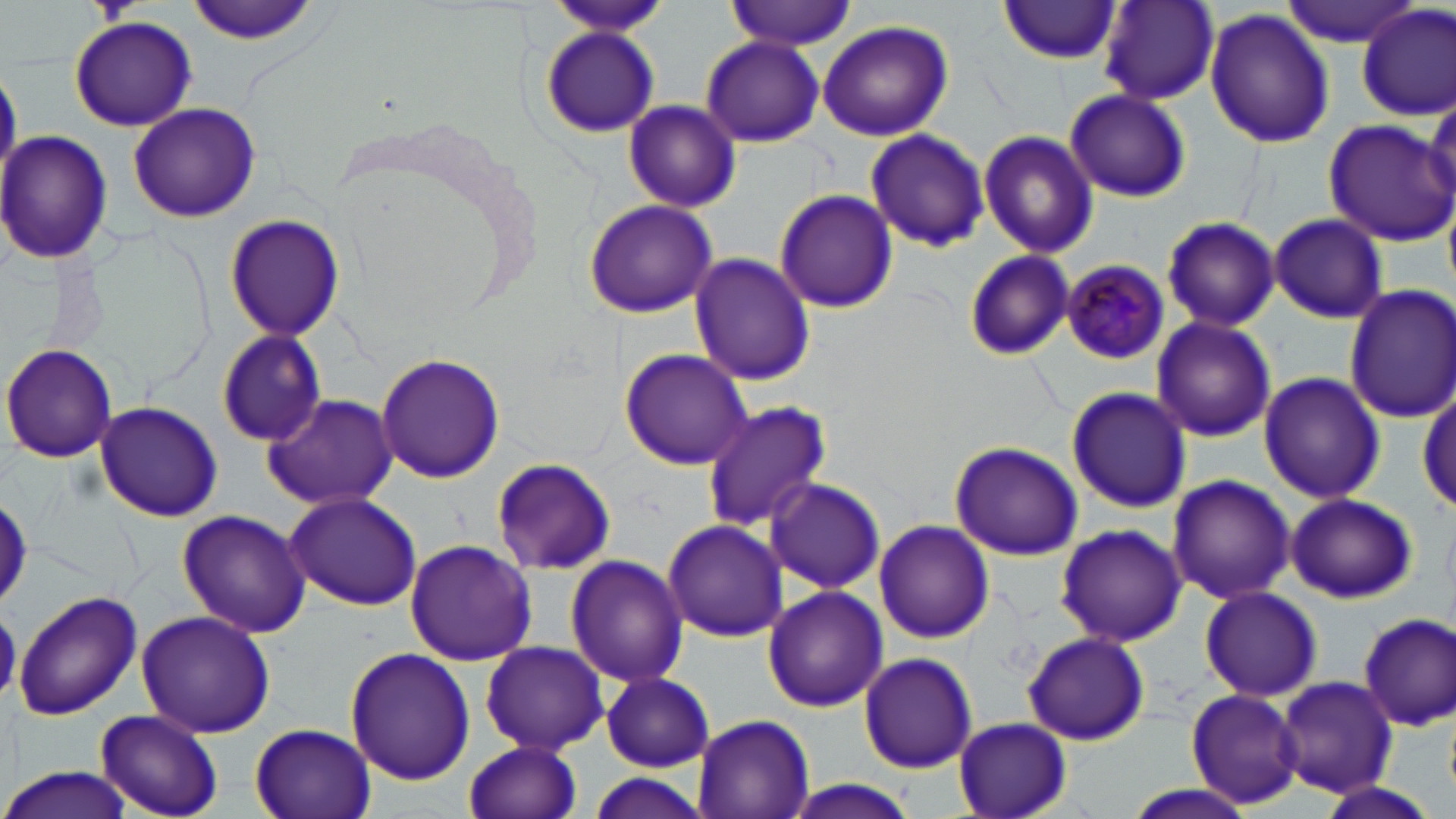 Approximate bounding boxes as named x1/y1/x2/y2 corners in pixels. Plasmodium malariae-infected red blood cell locations: (x1=1060, y1=260, x2=1168, y2=365). Uninfected red blood cell locations: (x1=183, y1=0, x2=323, y2=45), (x1=727, y1=0, x2=854, y2=51), (x1=1281, y1=0, x2=1423, y2=46), (x1=997, y1=1, x2=1122, y2=65), (x1=553, y1=2, x2=671, y2=36), (x1=1098, y1=3, x2=1220, y2=105), (x1=1357, y1=5, x2=1455, y2=121), (x1=1205, y1=9, x2=1335, y2=148), (x1=70, y1=16, x2=196, y2=131), (x1=817, y1=21, x2=953, y2=141), (x1=540, y1=27, x2=660, y2=139), (x1=699, y1=36, x2=825, y2=148), (x1=0, y1=65, x2=21, y2=185), (x1=1064, y1=88, x2=1191, y2=203), (x1=623, y1=100, x2=740, y2=212), (x1=126, y1=102, x2=261, y2=224), (x1=1322, y1=120, x2=1456, y2=247), (x1=865, y1=129, x2=990, y2=251), (x1=0, y1=131, x2=114, y2=265), (x1=979, y1=131, x2=1099, y2=258), (x1=774, y1=189, x2=898, y2=313), (x1=582, y1=199, x2=718, y2=319), (x1=223, y1=212, x2=344, y2=342), (x1=1269, y1=214, x2=1388, y2=321), (x1=1161, y1=215, x2=1282, y2=332), (x1=960, y1=249, x2=1076, y2=360), (x1=689, y1=252, x2=815, y2=387), (x1=1343, y1=283, x2=1456, y2=424), (x1=1151, y1=316, x2=1277, y2=443), (x1=216, y1=328, x2=327, y2=445), (x1=1, y1=343, x2=118, y2=463), (x1=618, y1=348, x2=751, y2=469), (x1=375, y1=353, x2=506, y2=484), (x1=1258, y1=371, x2=1386, y2=504), (x1=1066, y1=386, x2=1192, y2=514), (x1=262, y1=393, x2=401, y2=512), (x1=1415, y1=394, x2=1455, y2=515), (x1=93, y1=401, x2=223, y2=521), (x1=700, y1=401, x2=832, y2=532), (x1=951, y1=442, x2=1082, y2=560), (x1=489, y1=456, x2=616, y2=575), (x1=1166, y1=473, x2=1295, y2=605), (x1=764, y1=476, x2=885, y2=594), (x1=283, y1=491, x2=422, y2=611), (x1=1285, y1=492, x2=1417, y2=603), (x1=0, y1=493, x2=31, y2=611), (x1=177, y1=509, x2=311, y2=638), (x1=661, y1=519, x2=787, y2=642), (x1=875, y1=519, x2=992, y2=645), (x1=1054, y1=523, x2=1185, y2=647), (x1=405, y1=539, x2=536, y2=665), (x1=564, y1=555, x2=689, y2=688), (x1=1199, y1=585, x2=1322, y2=701), (x1=762, y1=586, x2=887, y2=712), (x1=13, y1=591, x2=143, y2=722), (x1=135, y1=609, x2=276, y2=739), (x1=1357, y1=613, x2=1456, y2=730), (x1=1023, y1=630, x2=1149, y2=746), (x1=477, y1=643, x2=611, y2=754), (x1=343, y1=647, x2=476, y2=784), (x1=858, y1=651, x2=978, y2=773), (x1=601, y1=672, x2=713, y2=772), (x1=1276, y1=676, x2=1396, y2=797), (x1=1186, y1=686, x2=1307, y2=810), (x1=94, y1=710, x2=224, y2=817), (x1=692, y1=713, x2=815, y2=819), (x1=952, y1=716, x2=1072, y2=819), (x1=250, y1=724, x2=374, y2=819), (x1=463, y1=738, x2=583, y2=819), (x1=0, y1=764, x2=138, y2=819), (x1=579, y1=774, x2=714, y2=818), (x1=1310, y1=779, x2=1446, y2=819), (x1=782, y1=780, x2=922, y2=819), (x1=1116, y1=784, x2=1261, y2=819). Slide-level diagnosis: Plasmodium malariae. Light microscopy. One field of a larger specimen. May-Grünwald-Giemsa-stained preparation. Captured at 1000x magnification. Image is 1456×819 pixels. Thin blood smear.